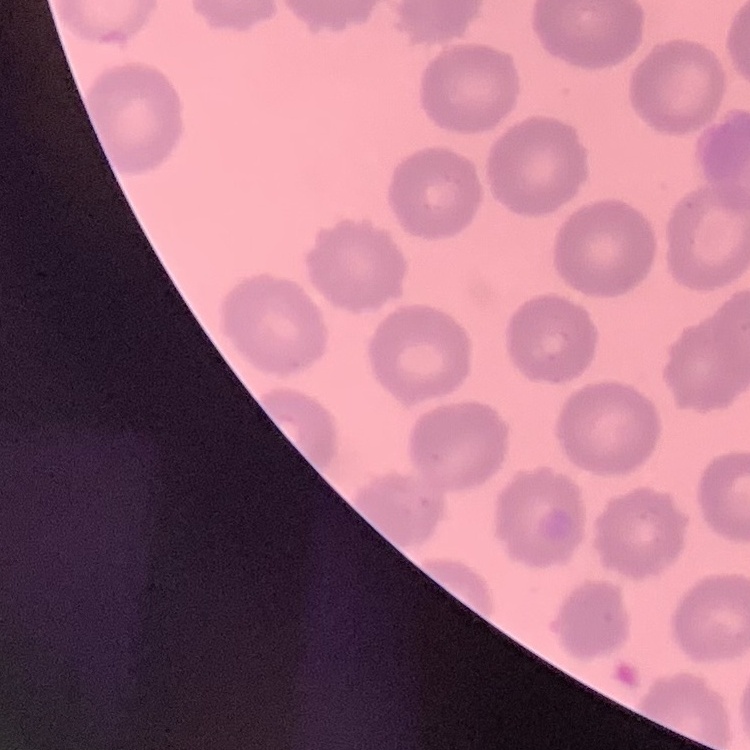
The red blood cells show no rouleaux formation. Field's or Giemsa stain. Square crop of a larger photomicrograph. Thin peripheral smear.